Mark where leukocytes are.
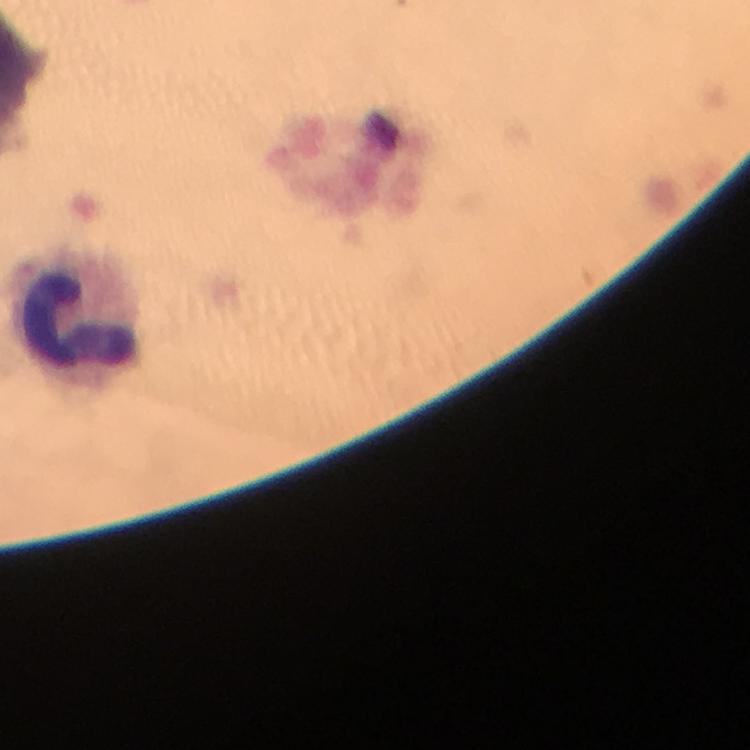

Approximate object centers, in pixels from the top-left corner.
Leukocytes: (x=76, y=316).

Thick blood smear. Giemsa stain. Photographed through the microscope with a smartphone camera. At 100x magnification. Plasmodium parasites: none detected. Cropped region of a single field of view. Image is 750×750 pixels. Immersion oil applied. From a diagnostic examination for malaria.